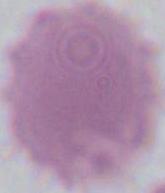
Summary:
  - Modality: micrograph
  - Magnification: 1000x
  - Identification: red blood cell